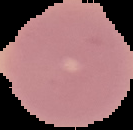
From a thin blood smear. Malaria status: uninfected. Image is 133×130 pixels. The area outside the segmented cell region is set to black.